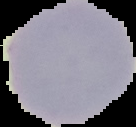

result: no malaria parasites seen
preparation: thin blood smear
image_size: 136×127 pixels
image_type: segmented cell region with the area outside set to black